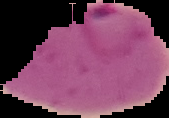
Summary:
  - Image size: 169×118 pixels
  - Preparation: thin blood smear
  - Malaria status: parasitized
  - Image type: cell region segmented out of the field of view; surrounding area masked to black